Assess this cell for malaria.
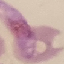

Parasitized.

Summary:
  - Stain: Giemsa
  - Preparation: thin blood smear
  - Image type: cell patch, automatically extracted from a larger field of view and resized to 64 × 64 pixels
  - Capture: smartphone camera at the microscope eyepiece